State which parasite is depicted.
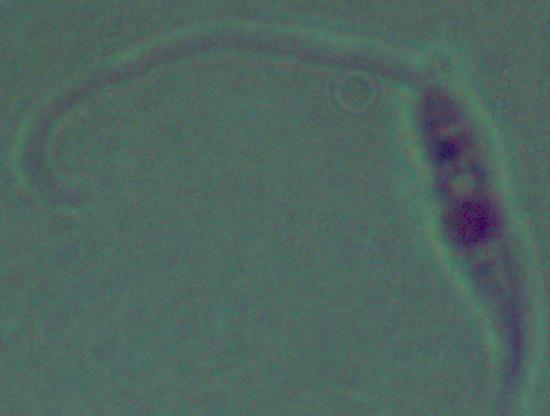
Leishmania.

magnification = 1000x
modality = micrograph